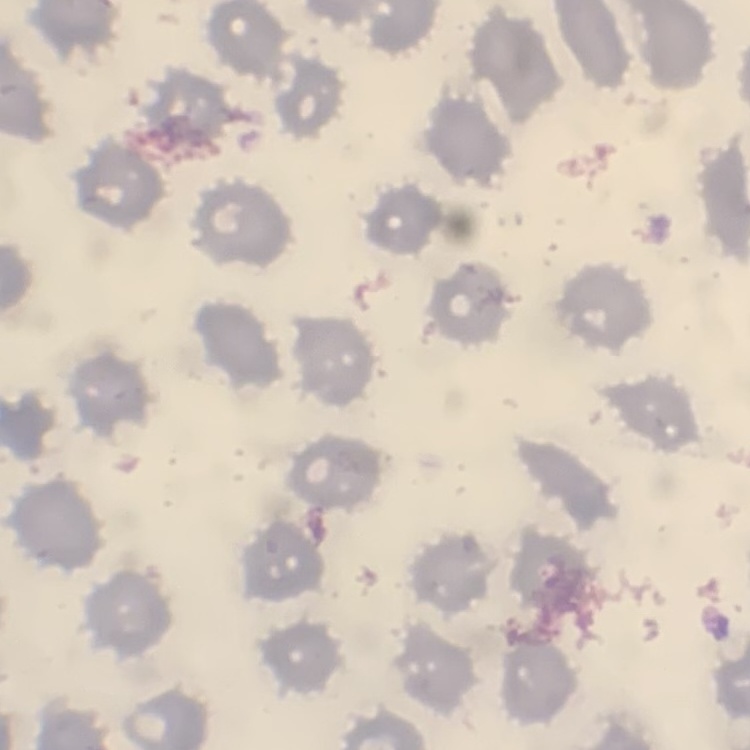

erythrocyte_morphology: no rouleaux formation
image_type: square crop of a larger photomicrograph
stain: Field's or Giemsa
preparation: thin peripheral smear